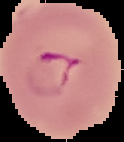

Summary:
  - Preparation: thin blood smear
  - Image size: 124×142 pixels
  - Result: Plasmodium parasites identified
  - Image type: segmented cell region on a black background